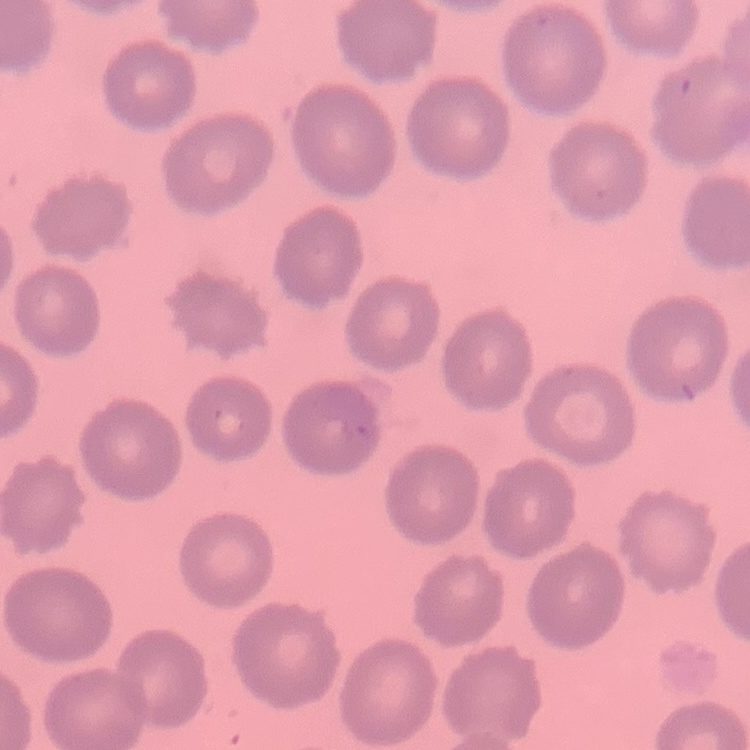
{
  "erythrocyte_morphology": "no rouleaux formation",
  "preparation": "thin blood film",
  "image_type": "square crop of a larger photomicrograph",
  "stain": "Field's or Giemsa"
}